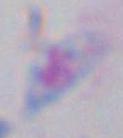
Summary:
  - Magnification: 1000x
  - Modality: photomicrograph
  - Identification: Toxoplasma gondii